Classify this cell by malaria status.
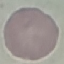
Uninfected.

Summary:
  - Capture: smartphone camera at the microscope eyepiece
  - Image type: cell patch, automatically extracted from a larger field of view and resized to 64 × 64 pixels
  - Stain: Giemsa
  - Preparation: thin blood smear